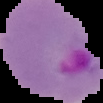
{
  "result": "Plasmodium parasites identified",
  "image_type": "segmented cell region on a black background",
  "preparation": "thin blood smear",
  "image_size": "103×103 pixels"
}